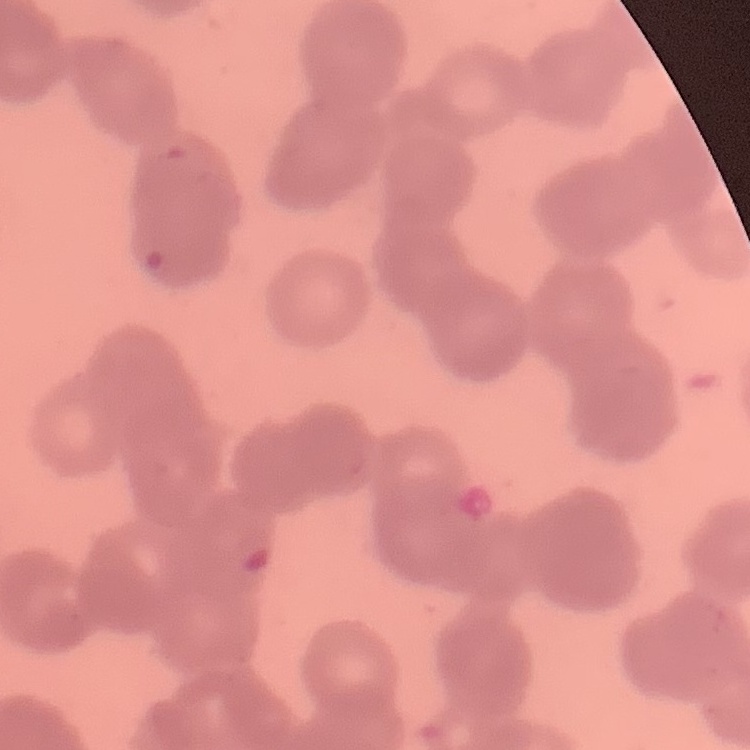
Summary:
  - Erythrocyte morphology: rouleaux formation
  - Stain: Field's or Giemsa
  - Preparation: thin blood film
  - Image type: square crop of a larger photomicrograph